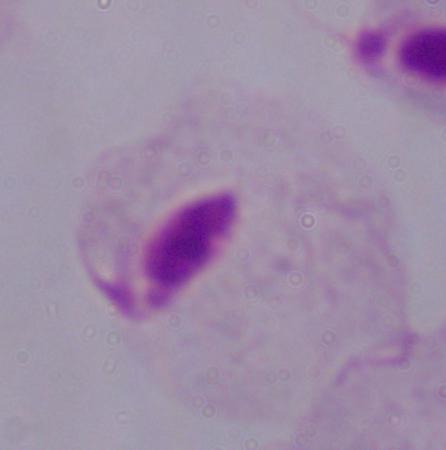
Summary:
  - Identification: trichomonad
  - Magnification: 1000x
  - Modality: photomicrograph